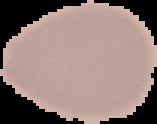 From a thin blood film. Image is 157×124 pixels. The area outside the segmented cell region is set to black. Result: no Plasmodium parasites seen.